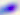
magnification = 400x
identification = Toxoplasma gondii
modality = micrograph